Identify the cell.
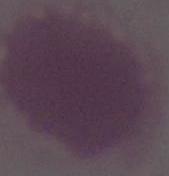

An erythrocyte.

Summary:
  - Magnification: 1000x
  - Modality: micrograph